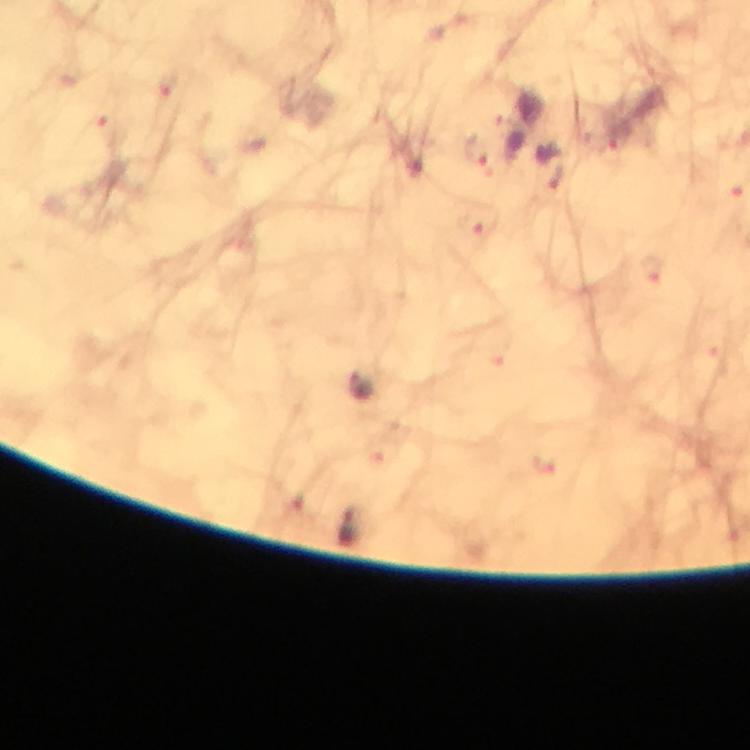

Approximate centers as {x, y} in pixels.
Summary:
  - Malaria parasite locations: {169, 84}, {617, 139}, {475, 152}, {476, 225}, {652, 269}, {362, 388}, {349, 527}
  - Preparation: thick smear
  - Immersion oil: applied
  - Image size: 750×750 pixels
  - Context: from a diagnostic examination for malaria
  - Magnification: 100x
  - Capture: smartphone camera through the microscope
  - Cropped from: a single field of view
  - Stain: Giemsa